Comment on the morphology of the red blood cells.
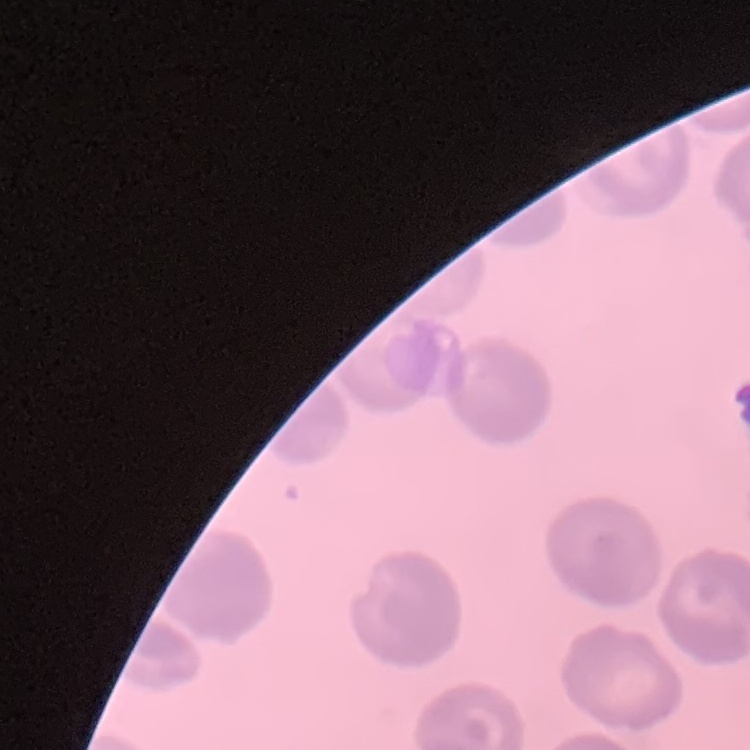

No rouleaux formation.

{
  "preparation": "thin peripheral smear",
  "image_type": "one tile cut from a larger photomicrograph",
  "stain": "Field's or Giemsa"
}